Identify the preparation type.
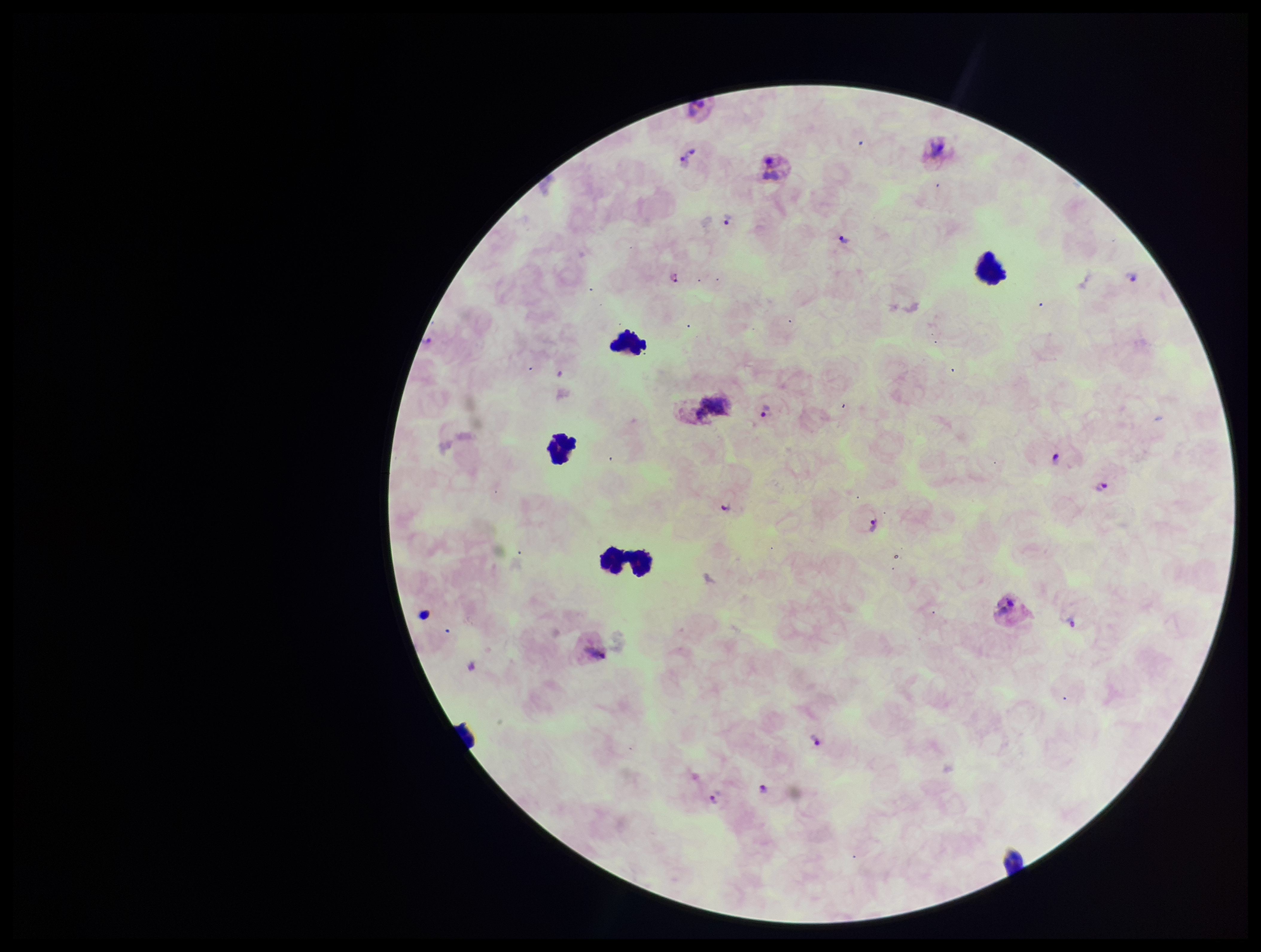

A thick smear.

Species reported for this patient: Plasmodium vivax. Image is 1261×952 pixels. Leukocyte count: 5. Single field of view. Parasite count: 12. Giemsa stain. Patient malaria status: infected. Plasmodium parasites: identified. Photographed through the microscope eyepiece with a smartphone camera.